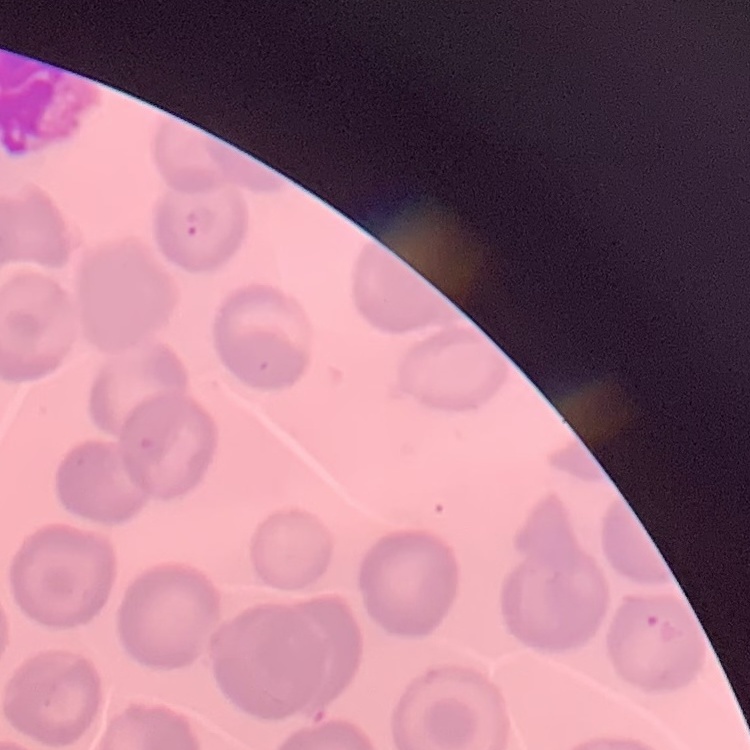

The red blood cells exhibit no rouleaux formation. Field's or Giemsa stain. Thin peripheral smear. Square crop of a larger photomicrograph.